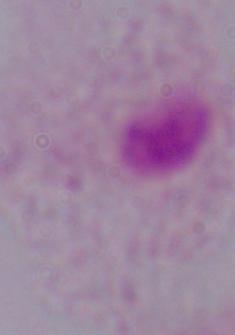 Photomicrograph. 1000x magnification. A trichomonad is seen.